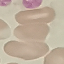
Summary:
  - Malaria status: uninfected
  - Capture: smartphone through the microscope eyepiece
  - Preparation: thin blood film
  - Image type: automatically extracted cell patch, resized to 64 × 64 pixels
  - Stain: Giemsa